Outline each blood parasite and name the species.
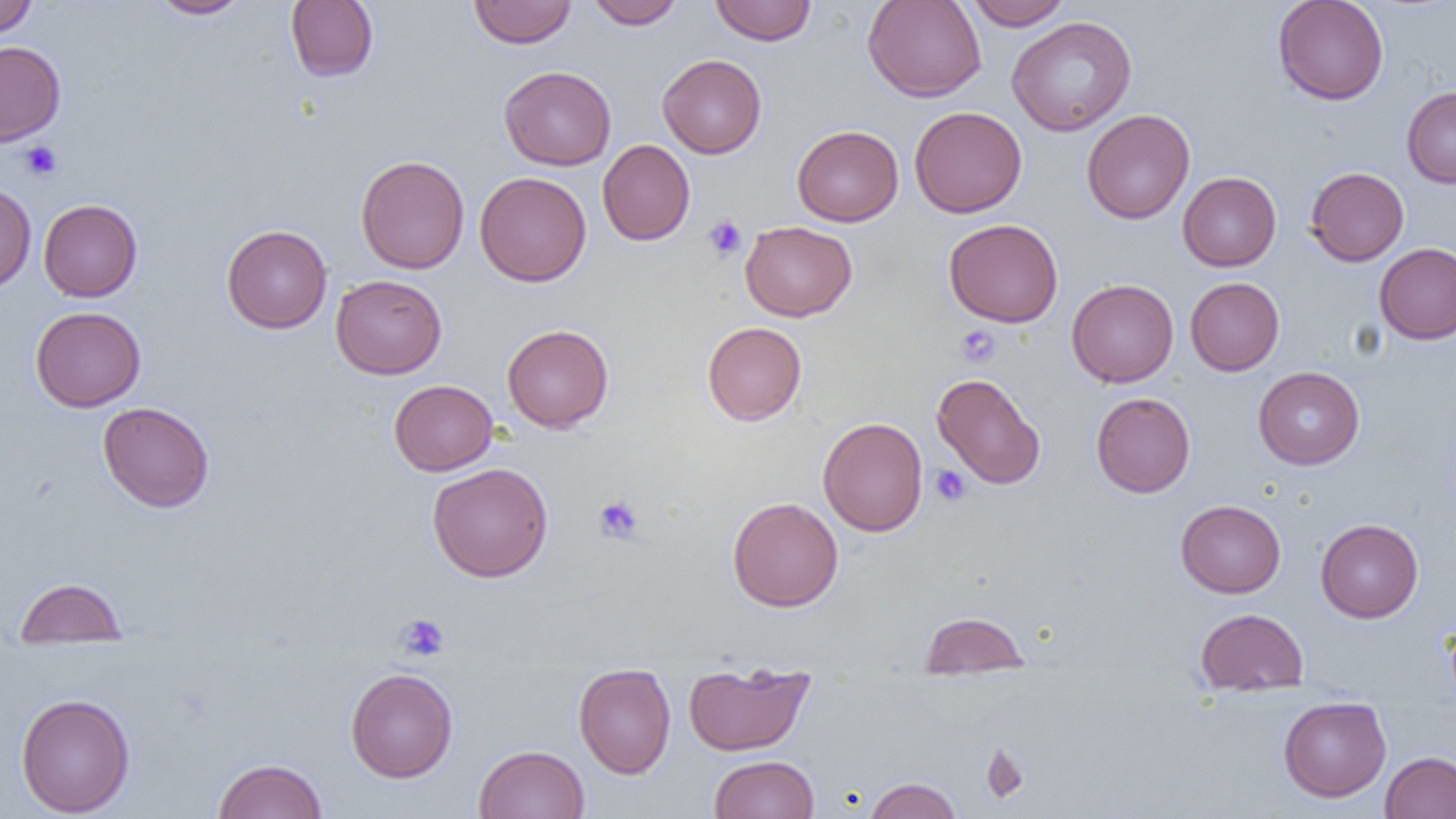
No blood parasites observed.

slide_level_diagnosis: negative for blood parasites
uninfected_red_blood_cell_locations: 'approximate bounding boxes as named x1/y1/x2/y2 corners in pixels: (x1=0, y1=0, x2=37, y2=38), (x1=147, y1=0, x2=251, y2=19), (x1=285, y1=0, x2=379, y2=82), (x1=468, y1=0, x2=576, y2=48), (x1=586, y1=0, x2=685, y2=29), (x1=862, y1=0, x2=987, y2=102), (x1=964, y1=0, x2=1072, y2=30), (x1=1272, y1=0, x2=1389, y2=105), (x1=710, y1=1, x2=816, y2=45), (x1=1006, y1=16, x2=1137, y2=136), (x1=0, y1=41, x2=66, y2=145), (x1=657, y1=54, x2=767, y2=158), (x1=499, y1=65, x2=616, y2=171), (x1=1401, y1=86, x2=1456, y2=188), (x1=909, y1=106, x2=1027, y2=218), (x1=1081, y1=108, x2=1195, y2=224), (x1=791, y1=125, x2=904, y2=226), (x1=597, y1=139, x2=695, y2=246), (x1=355, y1=155, x2=469, y2=274), (x1=1305, y1=167, x2=1409, y2=266), (x1=474, y1=171, x2=591, y2=287), (x1=1178, y1=171, x2=1281, y2=271), (x1=0, y1=181, x2=37, y2=295), (x1=38, y1=199, x2=142, y2=302), (x1=944, y1=219, x2=1064, y2=327), (x1=740, y1=221, x2=856, y2=321), (x1=221, y1=224, x2=332, y2=333), (x1=1374, y1=242, x2=1456, y2=345), (x1=331, y1=274, x2=447, y2=379), (x1=1185, y1=277, x2=1284, y2=375), (x1=1067, y1=278, x2=1179, y2=387), (x1=30, y1=306, x2=145, y2=412), (x1=702, y1=321, x2=807, y2=426), (x1=502, y1=324, x2=614, y2=433), (x1=1253, y1=366, x2=1364, y2=469), (x1=932, y1=373, x2=1046, y2=490), (x1=388, y1=379, x2=498, y2=476), (x1=1091, y1=392, x2=1195, y2=498), (x1=98, y1=401, x2=215, y2=513), (x1=818, y1=417, x2=928, y2=536), (x1=427, y1=462, x2=553, y2=582), (x1=727, y1=497, x2=843, y2=612), (x1=1175, y1=499, x2=1286, y2=597), (x1=1315, y1=518, x2=1423, y2=623), (x1=15, y1=577, x2=126, y2=650), (x1=1195, y1=607, x2=1308, y2=696), (x1=918, y1=611, x2=1031, y2=679), (x1=683, y1=660, x2=814, y2=756), (x1=573, y1=662, x2=676, y2=778), (x1=345, y1=667, x2=458, y2=783), (x1=16, y1=693, x2=135, y2=817), (x1=1278, y1=696, x2=1392, y2=802), (x1=474, y1=744, x2=590, y2=819), (x1=1381, y1=751, x2=1456, y2=818), (x1=709, y1=755, x2=819, y2=818), (x1=213, y1=758, x2=327, y2=819), (x1=862, y1=777, x2=963, y2=819)'
magnification: 1000x
platelet_locations: 'approximate bounding boxes as named x1/y1/x2/y2 corners in pixels: (x1=21, y1=141, x2=62, y2=181), (x1=703, y1=215, x2=747, y2=261), (x1=956, y1=325, x2=1000, y2=367), (x1=930, y1=465, x2=971, y2=506), (x1=594, y1=496, x2=643, y2=544), (x1=396, y1=613, x2=450, y2=661)'
modality: optical microscopy
field_of_view: single
image_size: 1456×819 pixels
preparation: thin blood smear